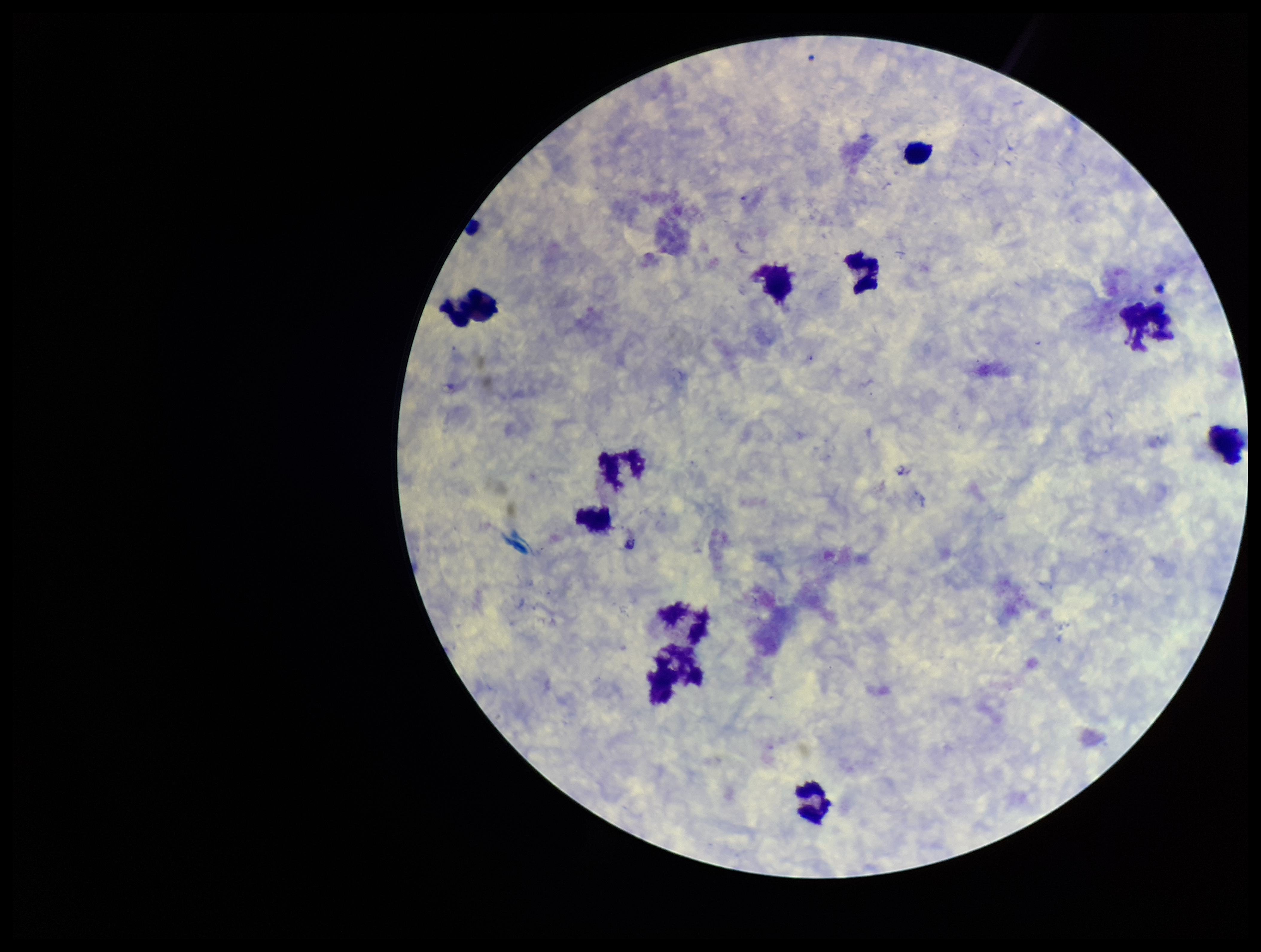 Smartphone photograph taken through the eyepiece of a microscope. Image is 1261×952 pixels. Preparation: thick. Parasite count: 0. Single field of view. Stained with Giemsa. Patient malaria status: negative. Leukocyte count: 11. Plasmodium parasites: none seen.